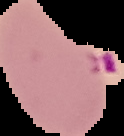 From a thin blood film. Malaria status: parasitized. Segmented cell region on a black background. Image is 124×136 pixels.